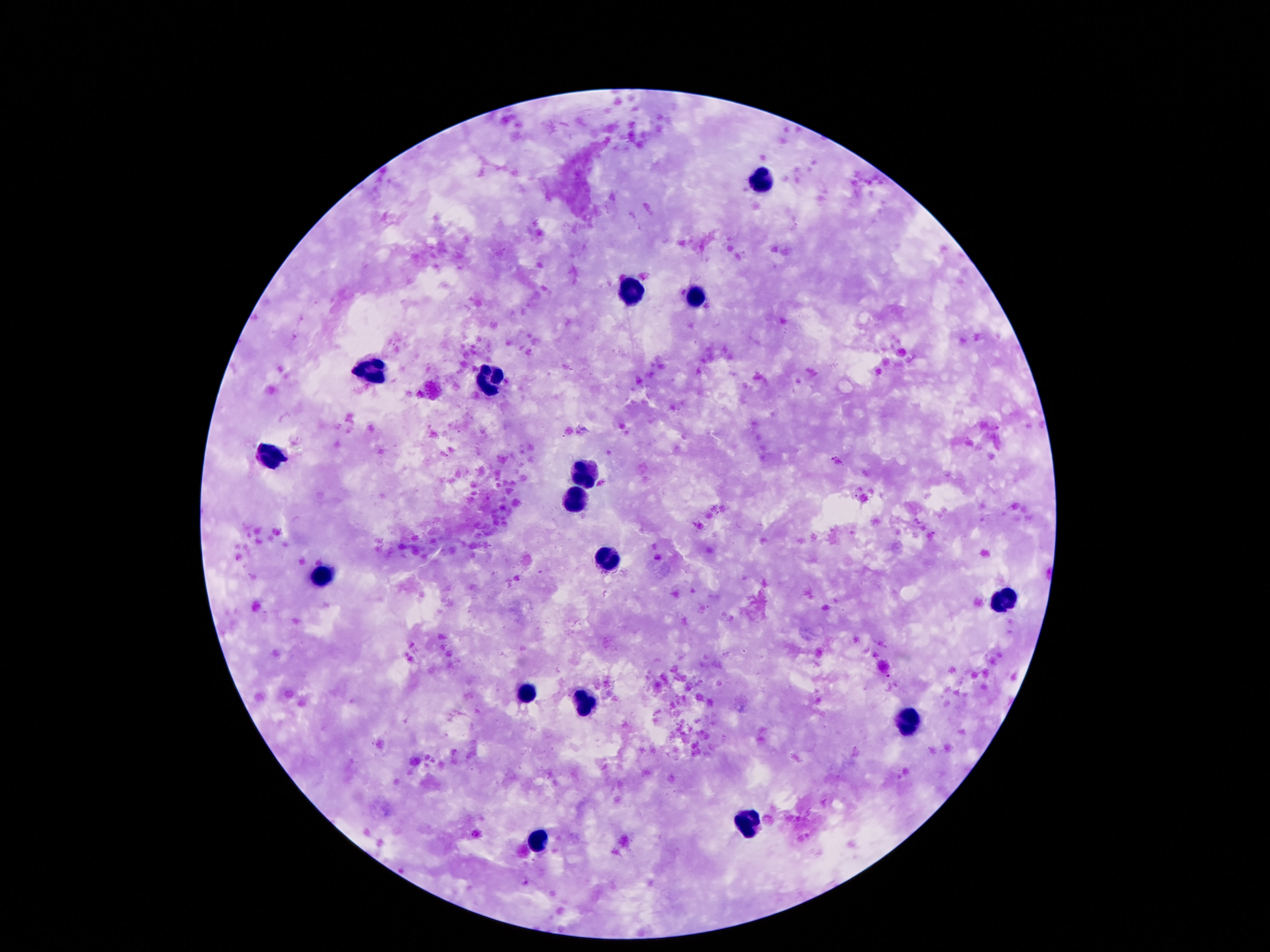
patient malaria status = negative
capture = smartphone camera through the microscope eyepiece
preparation = thick blood film
magnification = 100x
leukocyte locations = approximate object centers, in pixels from the top-left corner: (x=759, y=180), (x=628, y=294), (x=693, y=298), (x=370, y=371), (x=489, y=378), (x=268, y=455), (x=591, y=472), (x=573, y=497), (x=606, y=561), (x=326, y=577), (x=1004, y=603), (x=522, y=689), (x=582, y=704), (x=909, y=726), (x=750, y=822), (x=536, y=840)
image size = 1270×952 pixels
stain = Giemsa
field of view = single